Identify the parasite.
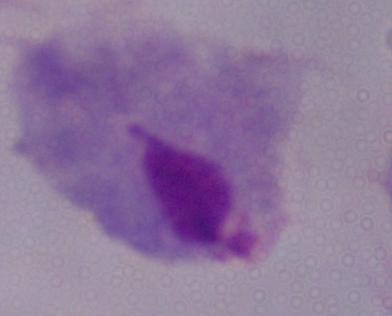

A trichomonad.

1000x magnification. Micrograph.